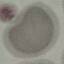
Result: no malaria parasites seen. Automatically extracted cell patch, resized to 64 × 64 pixels. Giemsa-stained preparation. Thin blood smear. Acquired by smartphone through the microscope eyepiece.